State the preparation type.
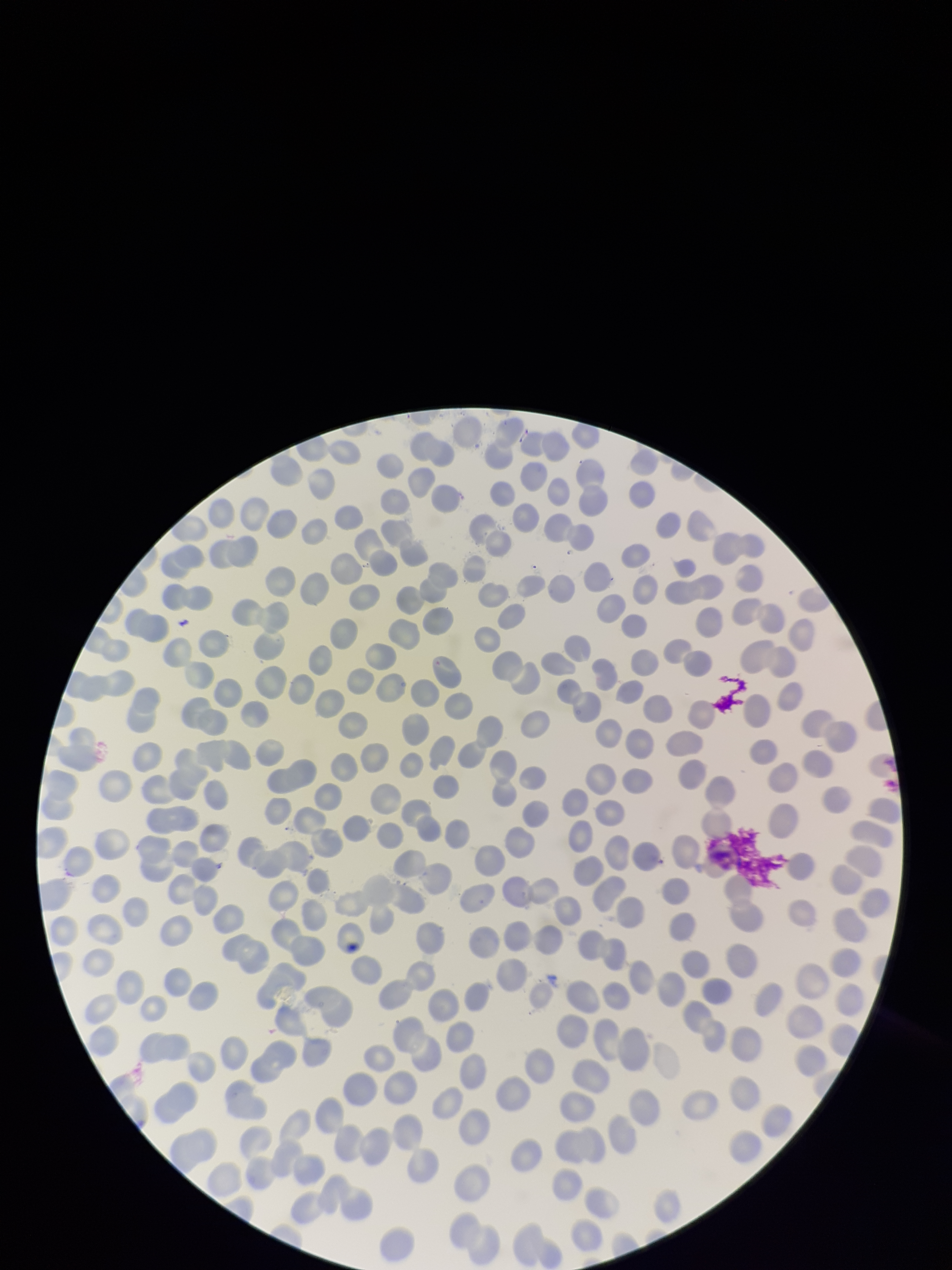
A thin smear.

Summary:
  - Capture: smartphone photograph through the microscope eyepiece
  - Parasitized red blood cell count: 0
  - Patient malaria status: negative
  - Field of view: one from this slide
  - Stain: Giemsa
  - Parasitized red blood cells: none identified
  - Image size: 952×1270 pixels
  - Red blood cell count: 294